Name the parasite shown.
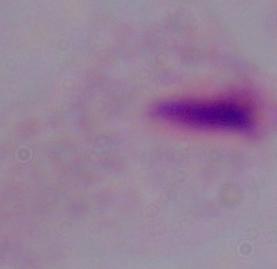
A trichomonad.

Summary:
  - Magnification: 1000x
  - Modality: photomicrograph